Assess this cell for malaria.
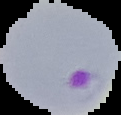

Parasitized.

image size = 121×115 pixels
image type = segmented cell region on a black background
preparation = thin blood smear